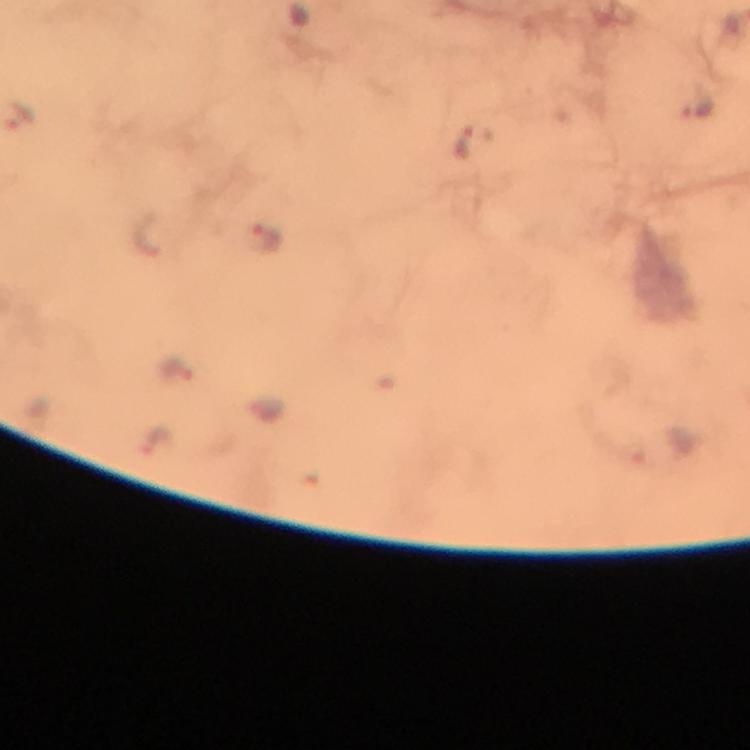

context = from a diagnostic examination for malaria
stain = Giemsa
magnification = 100x
capture = smartphone mounted on the microscope
image size = 750×750 pixels
cropped from = a single field of view
malaria parasite locations = approximate centers as (x, y) in pixels: (700, 99), (18, 114), (463, 145), (271, 239), (175, 369), (160, 442)
immersion oil = applied
preparation = thick blood film